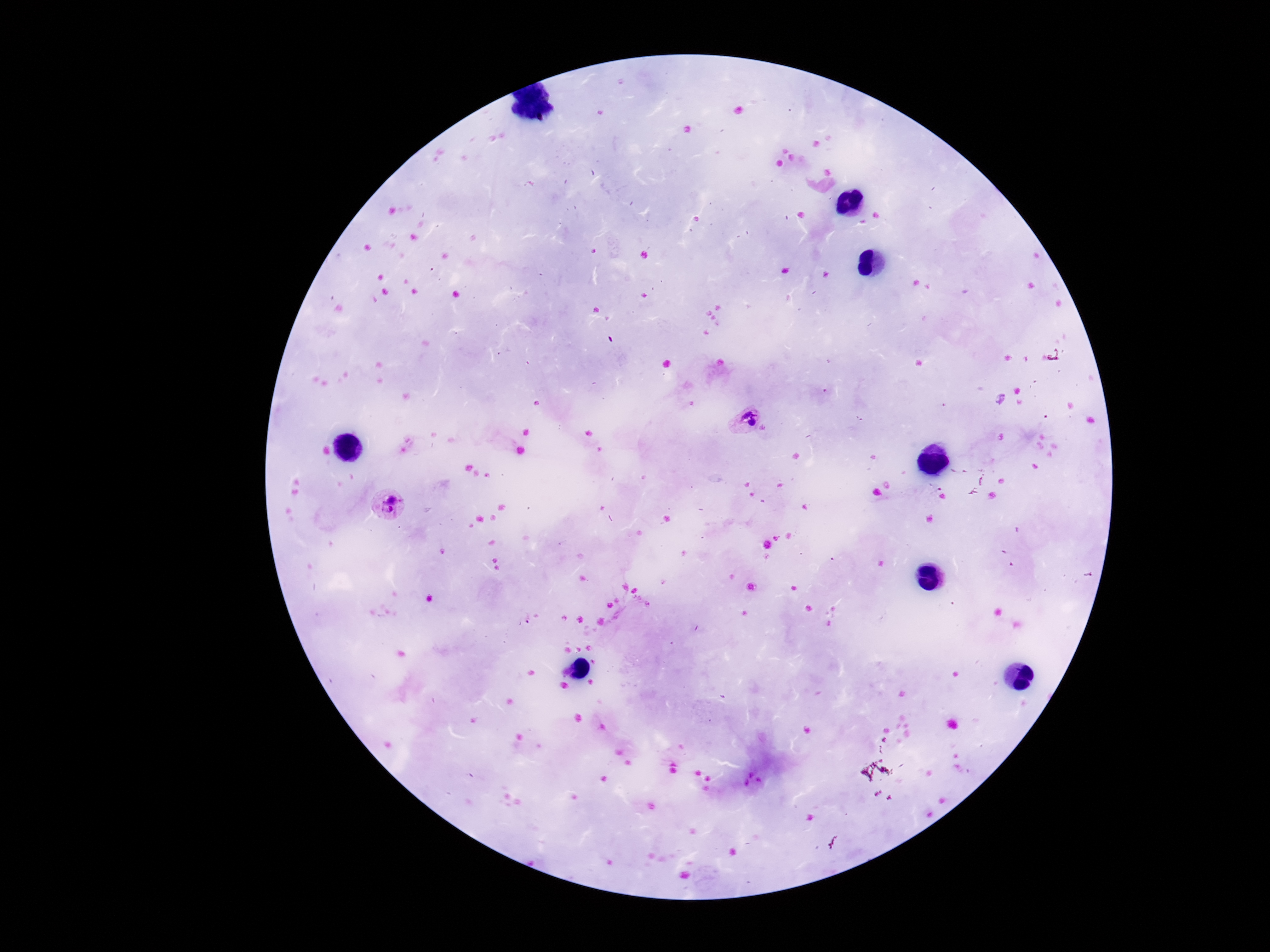
Approximate object centers, in pixels from the top-left corner.
Summary:
  - Plasmodium parasite locations: (x=742, y=418), (x=392, y=506)
  - Magnification: 100x
  - Image size: 1270×952 pixels
  - Patient malaria status: positive
  - Preparation: thick peripheral-blood smear
  - Capture: smartphone camera through the microscope eyepiece
  - Field of view: single
  - Stain: Giemsa